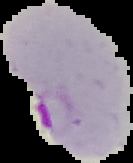

Summary:
  - Preparation: thin blood smear
  - Malaria status: parasitized
  - Image size: 133×163 pixels
  - Image type: segmented cell region with the area outside set to black